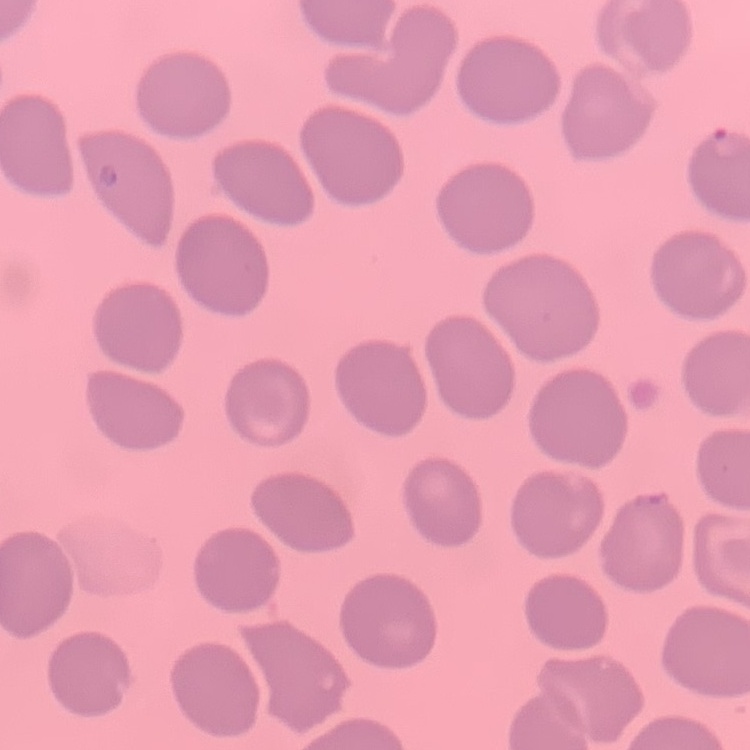
red_blood_cell_morphology: no rouleaux formation
preparation: thin blood smear
stain: Field's or Giemsa
image_type: square crop of a larger photomicrograph